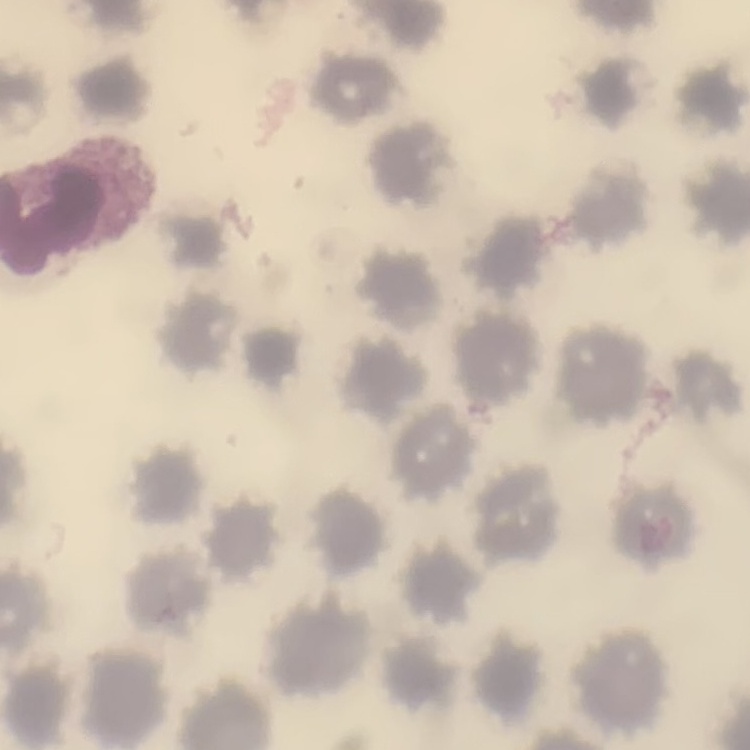

red blood cell morphology = no rouleaux formation
image type = square crop of a larger photomicrograph
stain = Field's or Giemsa
preparation = thin peripheral smear